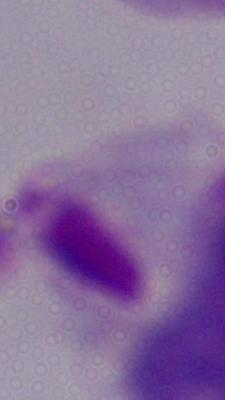

magnification = 1000x
identification = trichomonad
modality = photomicrograph